State which cell type is depicted.
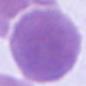
An erythrocyte.

Summary:
  - Modality: micrograph
  - Magnification: 1000x